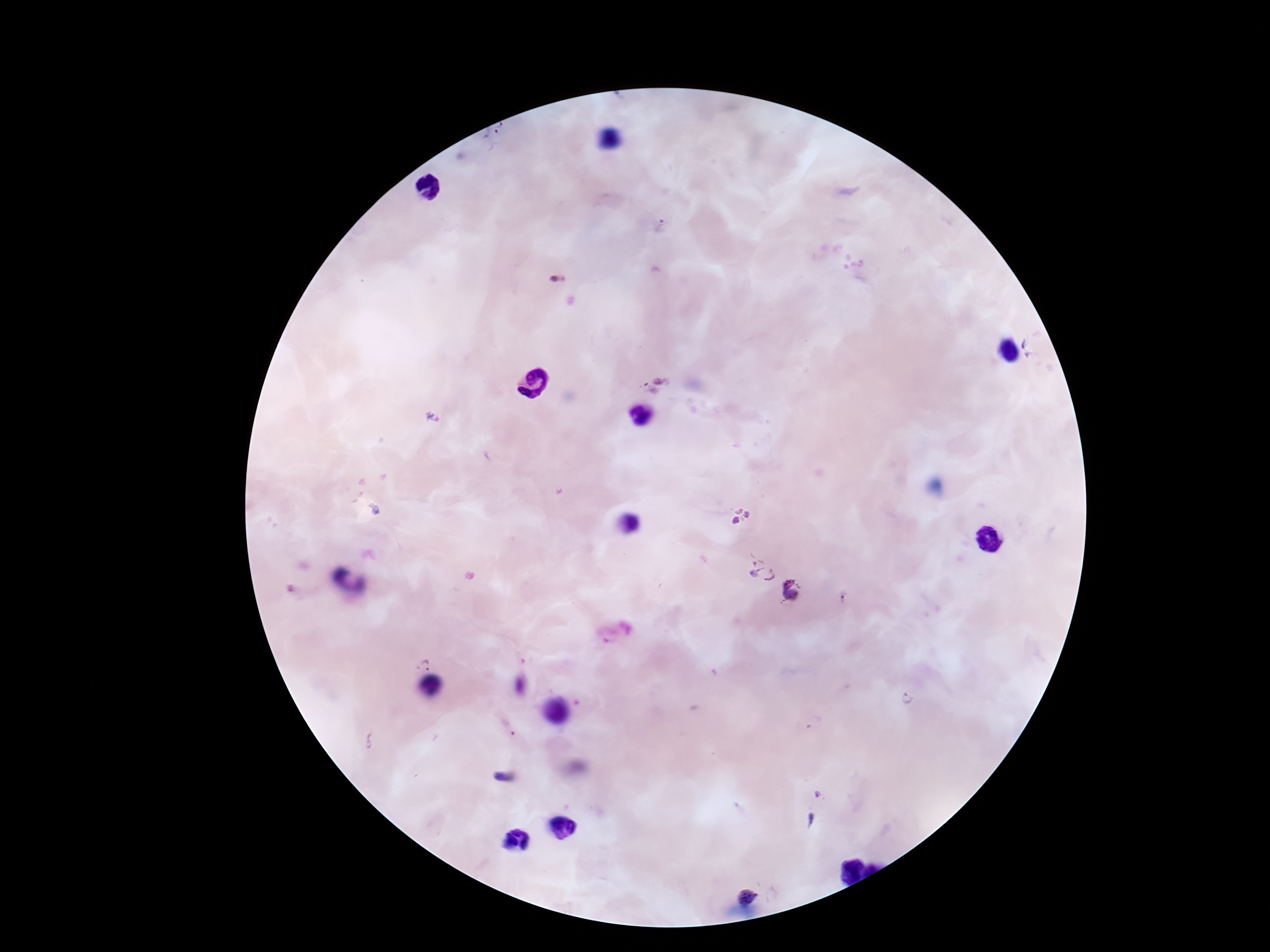

Approximate object centers, in pixels from the top-left corner.
Summary:
  - Plasmodium parasite locations: (x=496, y=143), (x=660, y=226), (x=1031, y=346), (x=654, y=383), (x=432, y=416), (x=741, y=515), (x=763, y=572), (x=790, y=592), (x=424, y=665), (x=906, y=699), (x=369, y=740), (x=746, y=896)
  - Capture: smartphone camera through the microscope eyepiece
  - Preparation: thick peripheral-blood smear
  - Image size: 1270×952 pixels
  - Field of view: one from this slide
  - Stain: Giemsa
  - Patient malaria status: positive
  - Magnification: 100x